Assess the morphology of the red blood cells.
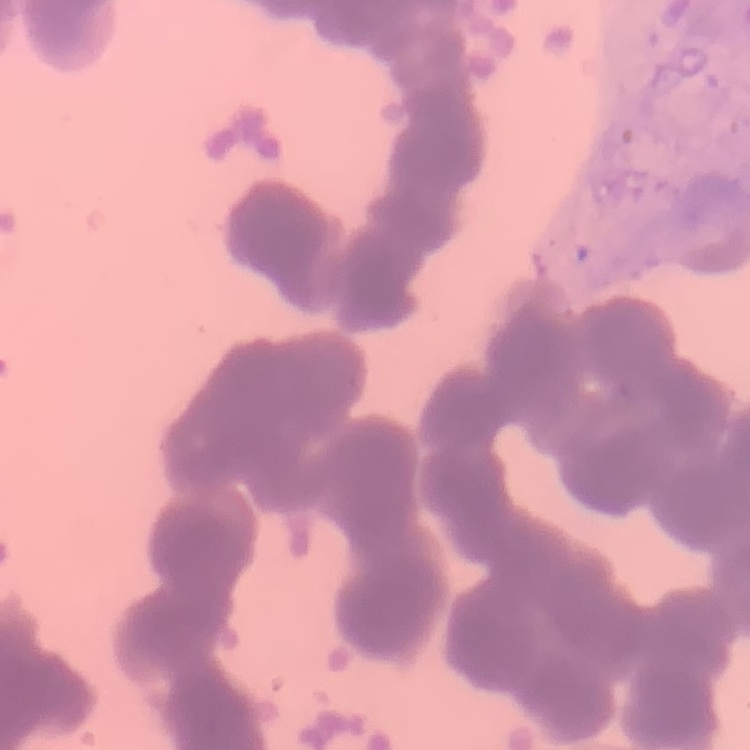
They show rouleaux formation.

Summary:
  - Preparation: thin peripheral smear
  - Stain: Field's or Giemsa
  - Image type: one tile cut from a larger photomicrograph